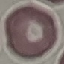
Malaria status: uninfected. Automatically extracted cell patch, resized to 64 × 64 pixels. Photographed with a smartphone camera at the microscope eyepiece. Thin blood film. Giemsa stain.